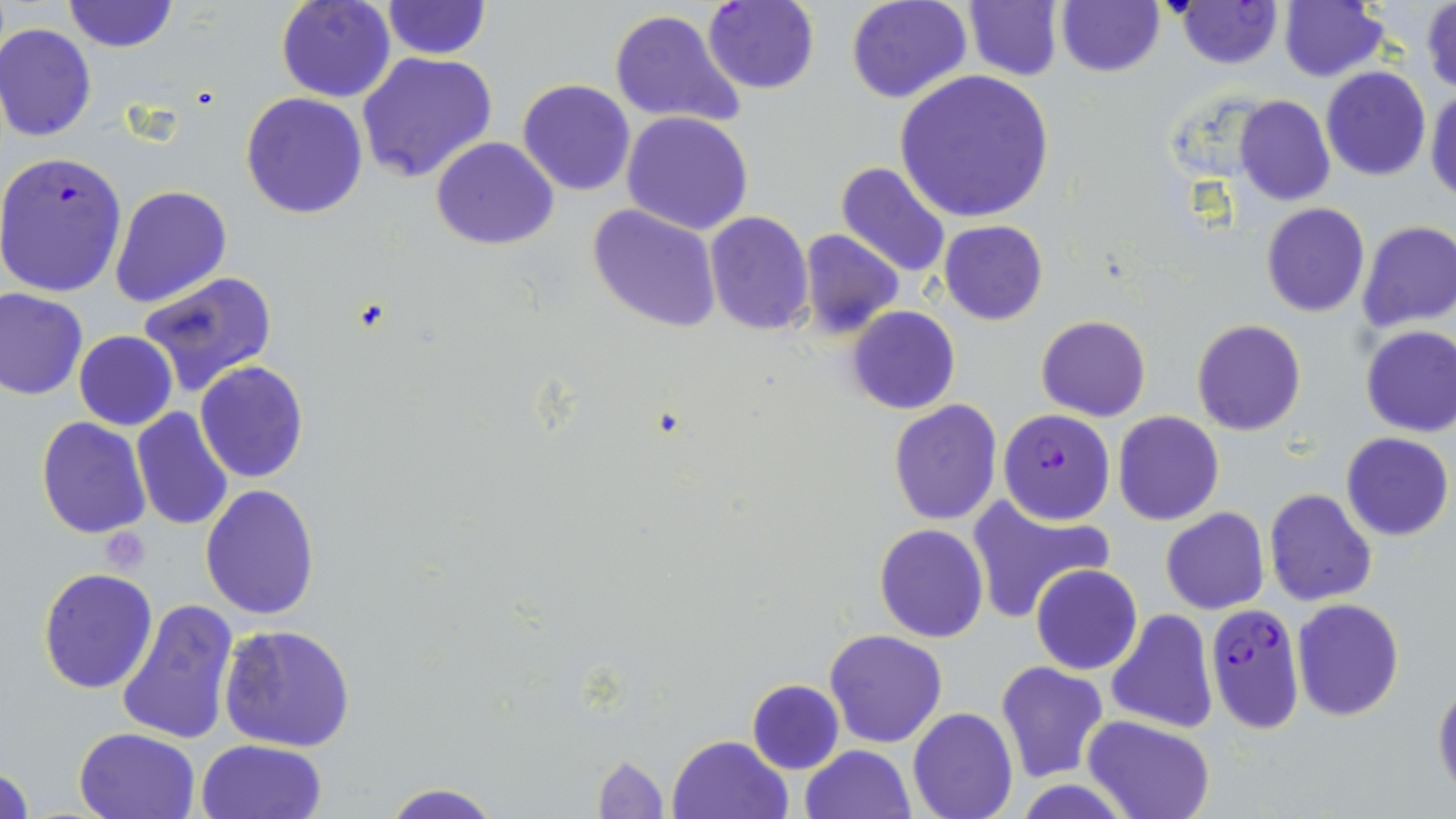

Summary:
  - Coordinate format: approximate bounding boxes as [x1, y1, x2, y2] in pixels
  - Plasmodium falciparum-infected red blood cell locations: [1174, 2, 1283, 69], [0, 150, 129, 299], [998, 409, 1115, 525], [1205, 602, 1304, 732]
  - Platelet locations: [102, 530, 151, 575]
  - Uninfected red blood cell locations: [61, 0, 179, 54], [276, 0, 397, 103], [381, 0, 490, 58], [846, 0, 972, 104], [962, 0, 1064, 82], [1054, 0, 1164, 77], [701, 1, 819, 95], [1279, 2, 1389, 81], [1422, 3, 1456, 94], [610, 9, 747, 129], [0, 22, 97, 141], [355, 50, 499, 184], [1320, 67, 1431, 181], [893, 69, 1057, 223], [517, 79, 636, 197], [1426, 88, 1456, 203], [240, 92, 369, 219], [1235, 97, 1336, 206], [622, 111, 753, 234], [431, 136, 558, 250], [835, 160, 954, 280], [110, 185, 232, 310], [1261, 203, 1369, 317], [588, 204, 721, 333], [705, 211, 814, 336], [938, 219, 1049, 326], [1358, 221, 1456, 332], [799, 228, 904, 339], [138, 271, 279, 397], [0, 287, 88, 399], [847, 305, 961, 415], [1036, 316, 1151, 420], [1191, 319, 1307, 436], [1359, 325, 1456, 438], [74, 331, 177, 430], [194, 361, 309, 483], [888, 399, 1003, 525], [131, 407, 234, 531], [1114, 411, 1224, 526], [35, 417, 152, 539], [1341, 431, 1453, 541], [200, 483, 320, 618], [1263, 489, 1377, 606], [967, 493, 1112, 622], [1161, 507, 1270, 614], [873, 522, 990, 642], [1031, 564, 1142, 676], [38, 567, 158, 694], [115, 598, 238, 746], [1290, 598, 1405, 721], [1104, 609, 1218, 734], [220, 624, 356, 751], [823, 629, 947, 748], [995, 662, 1109, 783], [1433, 678, 1455, 800], [746, 679, 844, 774], [908, 708, 1017, 819], [1084, 716, 1216, 819], [73, 726, 200, 818], [667, 733, 794, 819], [196, 738, 328, 819], [799, 744, 916, 819], [590, 754, 669, 818], [1, 762, 34, 819], [1011, 780, 1139, 817], [377, 782, 506, 819]
  - Slide-level diagnosis: Plasmodium falciparum
  - Stain: May-Grünwald-Giemsa
  - Modality: optical microscopy
  - Field of view: one of a larger specimen
  - Image size: 1456×819 pixels
  - Magnification: 1000x
  - Preparation: thin blood film